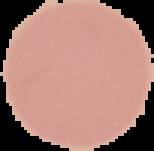
Result: no malaria parasites detected. The area outside the segmented cell region is set to black. From a thin blood smear. Image is 154×151 pixels.